Identify the parasite.
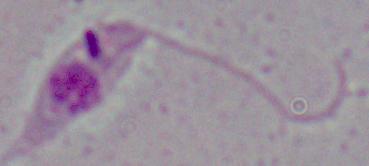

This is Leishmania.

magnification = 1000x
modality = photomicrograph